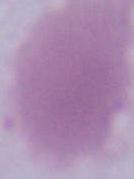

modality = micrograph
magnification = 1000x
identification = erythrocyte